Assess this cell for malaria.
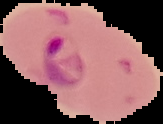
It is parasitized.

Summary:
  - Preparation: thin blood smear
  - Image size: 163×124 pixels
  - Image type: cell region segmented out of the field of view; surrounding area masked to black